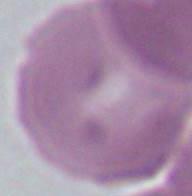

Summary:
  - Modality: micrograph
  - Magnification: 1000x
  - Identification: red blood cell